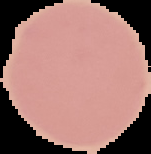

preparation = thin blood film
malaria status = uninfected
image type = cell region segmented out of the field of view; surrounding area masked to black
image size = 151×154 pixels